Describe the morphology of the erythrocytes.
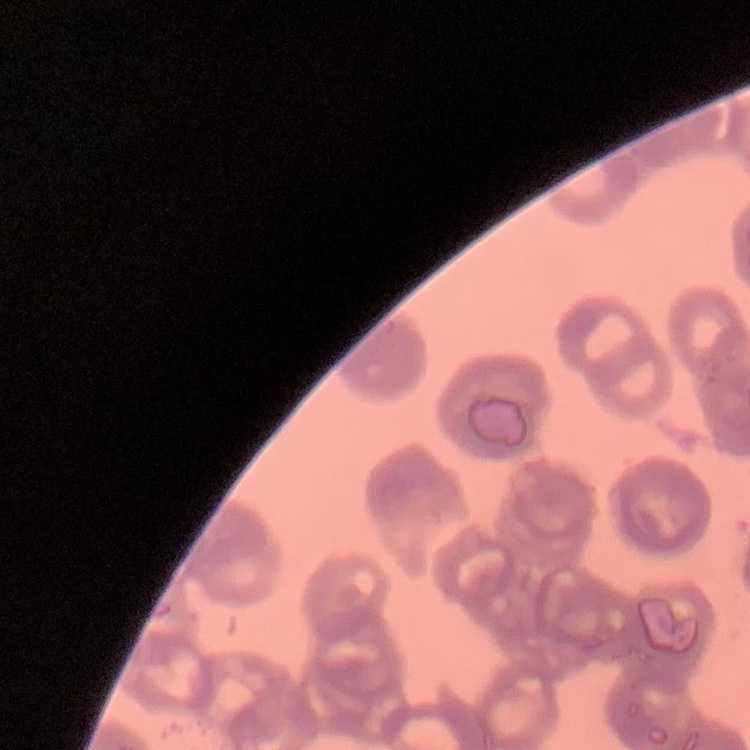

Rouleaux formation.

One tile cut from a larger photomicrograph. Thin peripheral smear. Stained with either Field's or Giemsa.